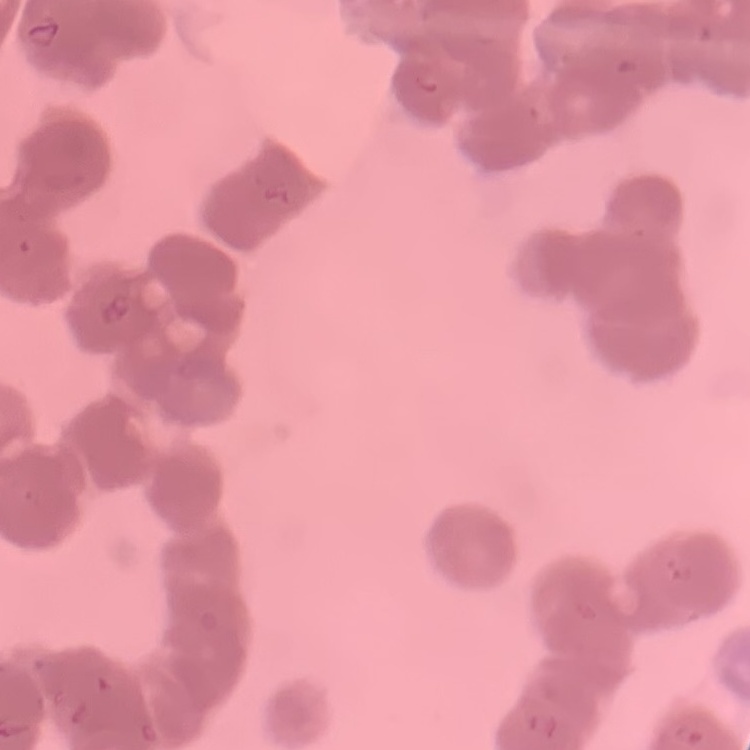

erythrocyte_morphology: rouleaux formation
image_type: square crop of a larger photomicrograph
preparation: thin blood film
stain: Field's or Giemsa